Classify this cell by malaria status.
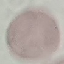
It is uninfected.

Summary:
  - Stain: Giemsa
  - Image type: cell patch, automatically extracted from a larger field of view and resized to 64 × 64 pixels
  - Preparation: thin blood film
  - Capture: smartphone through the microscope eyepiece